Describe the morphology of the red blood cells.
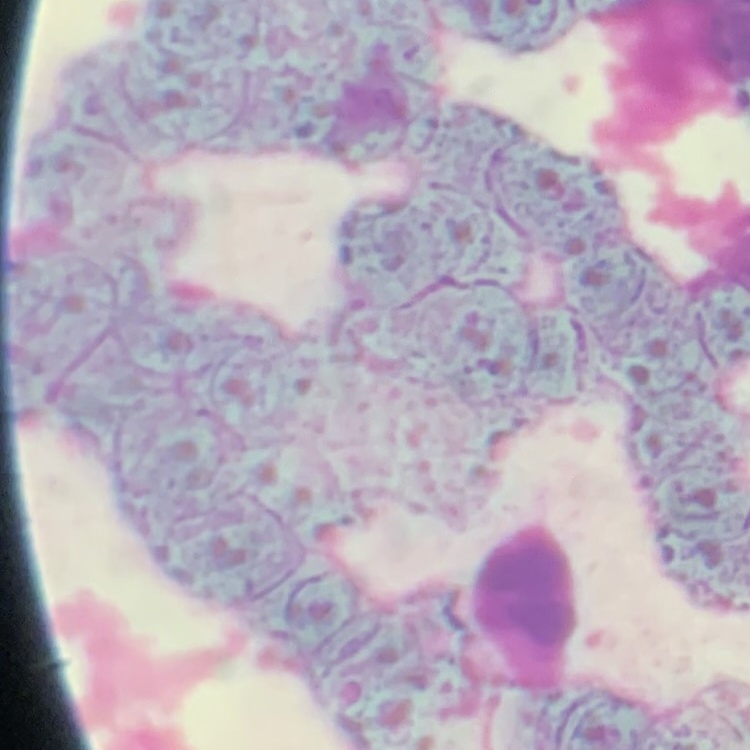
Rouleaux formation.

Summary:
  - Stain: Field's or Giemsa
  - Preparation: thin blood film
  - Image type: one tile cut from a larger photomicrograph